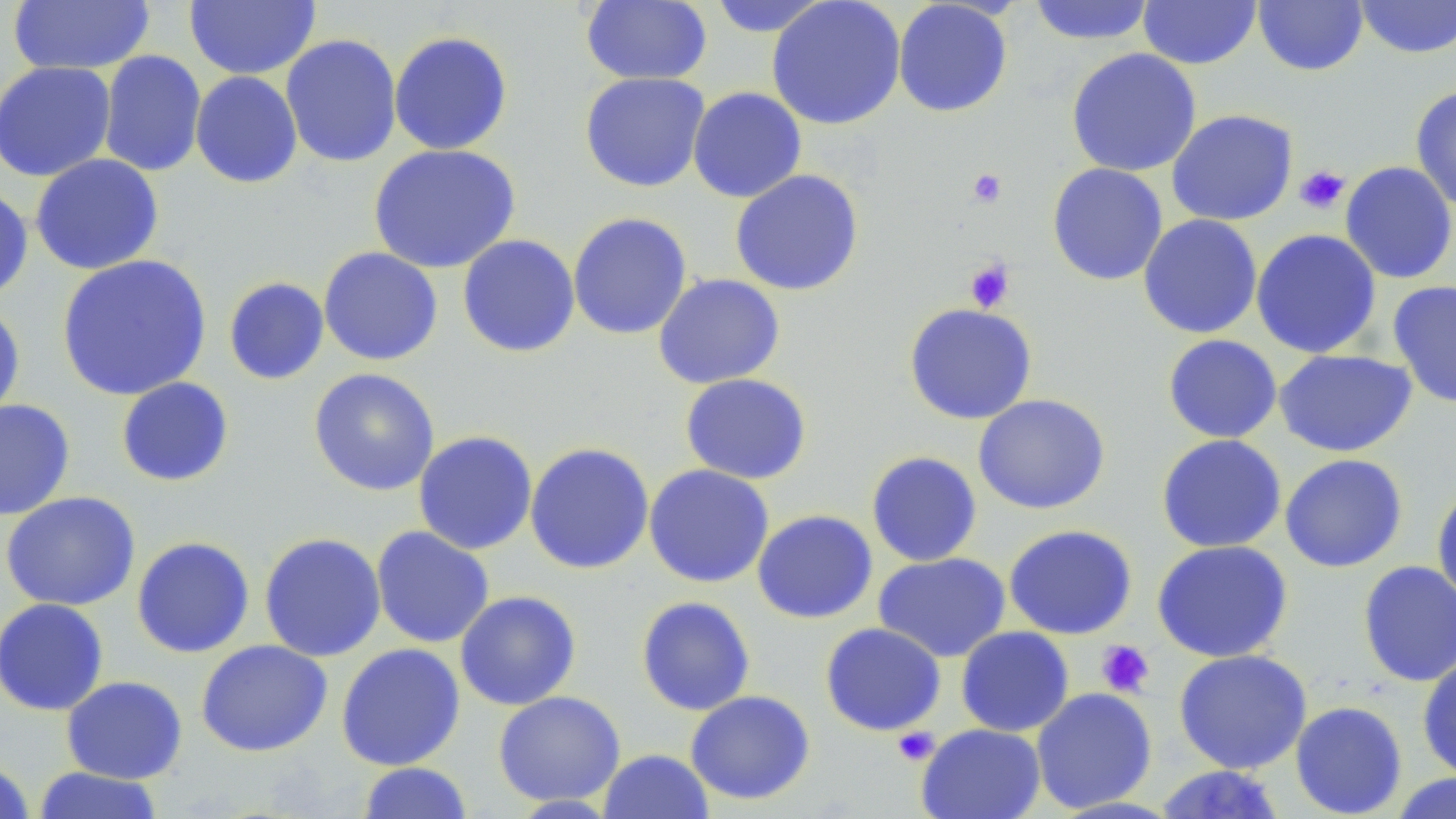

Summary:
  - Coordinate format: approximate bounding boxes as named x1/y1/x2/y2 corners in pixels
  - Uninfected red blood cell locations: (x1=580, y1=0, x2=712, y2=86), (x1=766, y1=0, x2=906, y2=130), (x1=1026, y1=0, x2=1158, y2=46), (x1=1138, y1=0, x2=1261, y2=69), (x1=1252, y1=0, x2=1369, y2=76), (x1=1354, y1=0, x2=1456, y2=59), (x1=8, y1=1, x2=155, y2=75), (x1=184, y1=1, x2=321, y2=80), (x1=706, y1=1, x2=836, y2=37), (x1=892, y1=1, x2=1013, y2=118), (x1=388, y1=30, x2=513, y2=156), (x1=280, y1=34, x2=402, y2=168), (x1=1065, y1=47, x2=1202, y2=177), (x1=97, y1=50, x2=207, y2=178), (x1=0, y1=61, x2=116, y2=182), (x1=190, y1=71, x2=303, y2=188), (x1=579, y1=72, x2=710, y2=193), (x1=1409, y1=85, x2=1456, y2=212), (x1=687, y1=86, x2=807, y2=203), (x1=1166, y1=109, x2=1298, y2=226), (x1=368, y1=143, x2=521, y2=274), (x1=30, y1=153, x2=165, y2=275), (x1=1339, y1=161, x2=1456, y2=284), (x1=1047, y1=162, x2=1168, y2=286), (x1=730, y1=169, x2=865, y2=296), (x1=0, y1=184, x2=33, y2=305), (x1=567, y1=212, x2=692, y2=340), (x1=1138, y1=214, x2=1263, y2=339), (x1=1251, y1=228, x2=1382, y2=359), (x1=457, y1=234, x2=581, y2=358), (x1=318, y1=246, x2=443, y2=366), (x1=56, y1=254, x2=212, y2=401), (x1=652, y1=273, x2=785, y2=389), (x1=222, y1=276, x2=329, y2=385), (x1=1387, y1=280, x2=1456, y2=408), (x1=0, y1=301, x2=26, y2=425), (x1=903, y1=302, x2=1038, y2=425), (x1=1162, y1=334, x2=1282, y2=443), (x1=1274, y1=348, x2=1418, y2=458), (x1=308, y1=368, x2=440, y2=496), (x1=679, y1=373, x2=813, y2=485), (x1=115, y1=377, x2=235, y2=487), (x1=972, y1=393, x2=1111, y2=515), (x1=0, y1=398, x2=75, y2=520), (x1=413, y1=430, x2=538, y2=555), (x1=1156, y1=434, x2=1287, y2=553), (x1=524, y1=442, x2=654, y2=575), (x1=866, y1=450, x2=983, y2=567), (x1=1279, y1=453, x2=1408, y2=573), (x1=643, y1=464, x2=774, y2=588), (x1=1431, y1=483, x2=1456, y2=607), (x1=0, y1=491, x2=140, y2=611), (x1=752, y1=510, x2=878, y2=624), (x1=1003, y1=523, x2=1138, y2=640), (x1=370, y1=525, x2=495, y2=649), (x1=259, y1=532, x2=386, y2=662), (x1=131, y1=536, x2=255, y2=658), (x1=1151, y1=540, x2=1294, y2=663), (x1=873, y1=552, x2=1011, y2=662), (x1=1357, y1=560, x2=1456, y2=687), (x1=454, y1=590, x2=582, y2=711), (x1=635, y1=596, x2=756, y2=716), (x1=0, y1=598, x2=110, y2=716), (x1=819, y1=622, x2=946, y2=736), (x1=955, y1=626, x2=1075, y2=737), (x1=196, y1=639, x2=333, y2=757), (x1=336, y1=643, x2=465, y2=771), (x1=1173, y1=649, x2=1312, y2=774), (x1=1416, y1=654, x2=1456, y2=781), (x1=61, y1=675, x2=187, y2=784), (x1=1031, y1=687, x2=1158, y2=813), (x1=685, y1=690, x2=816, y2=805), (x1=493, y1=691, x2=625, y2=807), (x1=1289, y1=700, x2=1408, y2=818), (x1=916, y1=723, x2=1046, y2=819), (x1=598, y1=749, x2=715, y2=819), (x1=0, y1=757, x2=35, y2=819), (x1=357, y1=762, x2=473, y2=819), (x1=1152, y1=765, x2=1288, y2=818), (x1=32, y1=766, x2=165, y2=818), (x1=1387, y1=773, x2=1456, y2=818)
  - Platelet locations: (x1=1294, y1=165, x2=1350, y2=215), (x1=966, y1=168, x2=1008, y2=209), (x1=964, y1=259, x2=1014, y2=313), (x1=1096, y1=640, x2=1154, y2=697), (x1=892, y1=726, x2=939, y2=766)
  - Slide-level diagnosis: negative for blood parasites
  - Field of view: single
  - Stain: May-Grünwald-Giemsa
  - Preparation: thin blood smear
  - Image size: 1456×819 pixels
  - Modality: optical microscopy
  - Magnification: 1000x